Name the cell type shown.
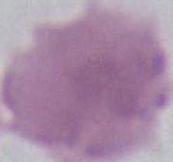

This is an erythrocyte.

Summary:
  - Magnification: 1000x
  - Modality: photomicrograph